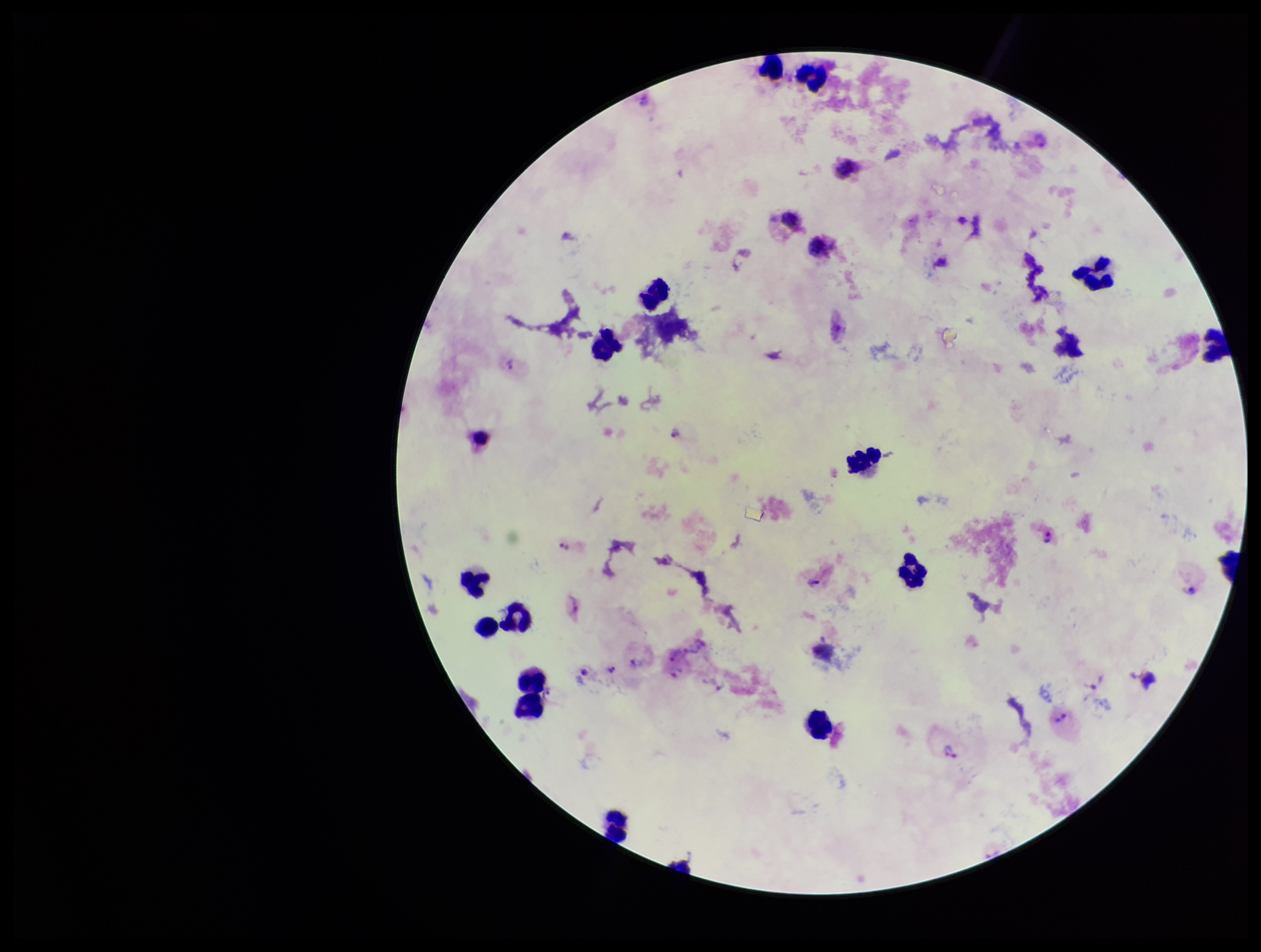
Parasite count: 13. One field from this slide. Preparation: thick smear. Smartphone photograph taken through the eyepiece of a microscope. Plasmodium parasites: detected. Leukocyte count: 21. Image is 1261×952 pixels. Species reported for this patient: Plasmodium vivax. Stained with Giemsa. Patient malaria status: positive.